Classify this cell by malaria status.
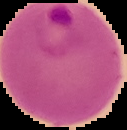
Parasitized.

Summary:
  - Image size: 127×130 pixels
  - Image type: segmented cell region with the area outside set to black
  - Preparation: thin blood smear